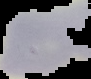
image size = 91×79 pixels
result = no Plasmodium parasites detected
preparation = thin blood film
image type = segmented cell region on a black background